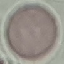 Malaria status: uninfected. Thin blood film. Giemsa stain. Cell patch, automatically extracted from a larger field of view and resized to 64 × 64 pixels. Acquired by smartphone through the microscope eyepiece.